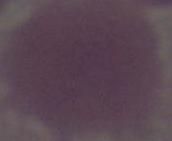 An erythrocyte is seen. Photomicrograph. Captured at 1000x magnification.